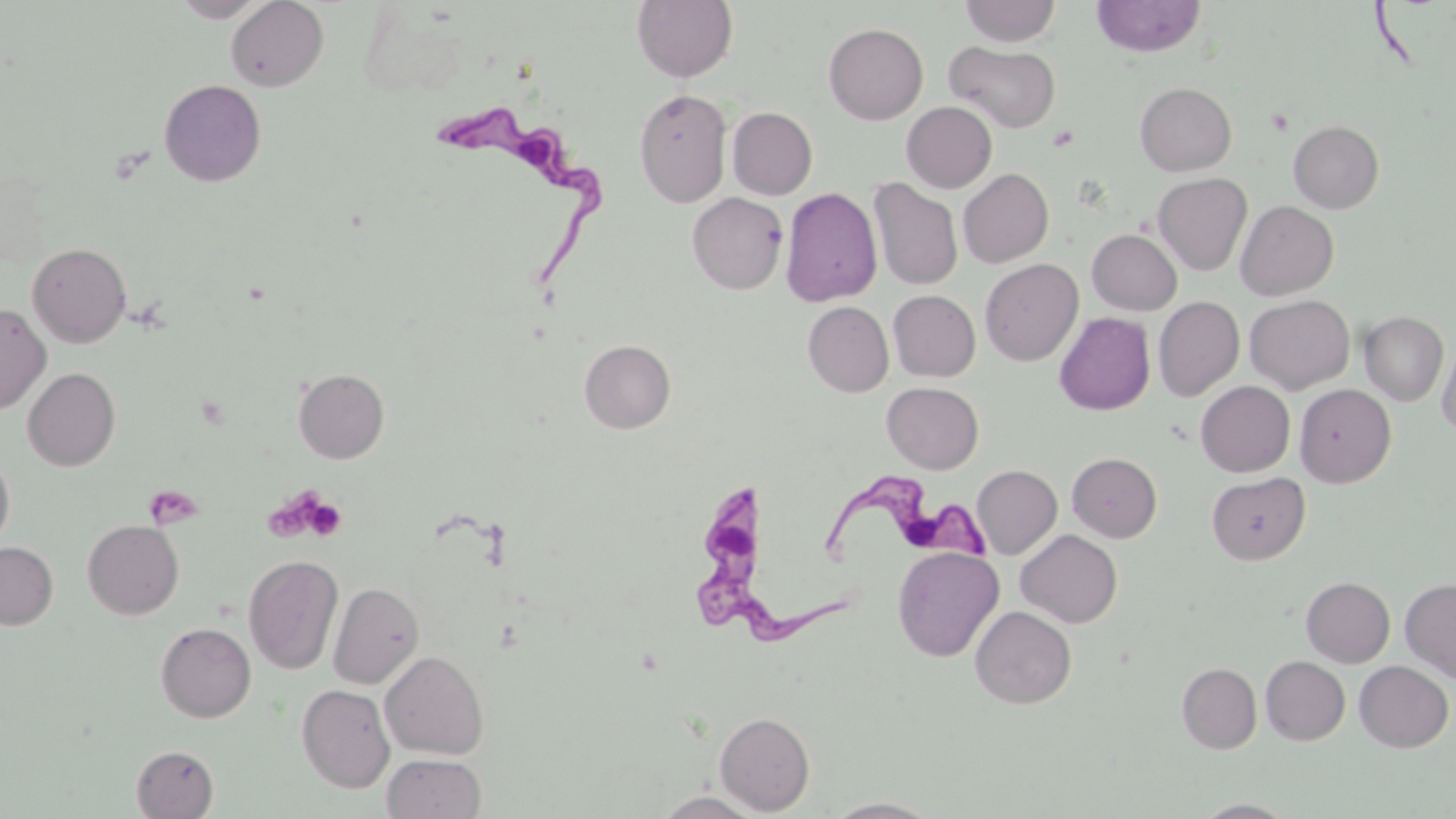
Summary:
  - Coordinate format: approximate bounding boxes as (x1, y1, x2, y2) in pixels
  - Uninfected red blood cell locations: (173, 0, 267, 22), (226, 0, 329, 91), (632, 0, 738, 83), (960, 0, 1061, 46), (1092, 0, 1206, 57), (824, 23, 928, 124), (944, 41, 1061, 133), (159, 79, 267, 187), (1135, 82, 1237, 176), (634, 88, 732, 208), (902, 101, 997, 192), (727, 107, 817, 200), (1288, 120, 1384, 213), (958, 168, 1053, 267), (1153, 173, 1252, 275), (869, 177, 963, 291), (780, 187, 882, 307), (687, 192, 788, 294), (1236, 200, 1339, 300), (1087, 229, 1182, 315), (27, 243, 131, 348), (980, 258, 1083, 366), (888, 290, 980, 381), (1244, 294, 1355, 394), (1153, 296, 1244, 401), (803, 301, 893, 397), (0, 303, 51, 414), (1054, 312, 1155, 415), (1359, 312, 1448, 406), (1437, 335, 1456, 437), (579, 339, 676, 433), (23, 367, 120, 471), (294, 368, 389, 463), (1196, 381, 1295, 477), (882, 382, 983, 473), (1294, 384, 1396, 487), (1067, 452, 1162, 542), (0, 453, 15, 551), (971, 464, 1062, 559), (1207, 472, 1310, 564), (83, 519, 183, 619), (1016, 529, 1122, 627), (0, 542, 58, 629), (892, 546, 1004, 662), (243, 554, 344, 674), (1302, 576, 1395, 667), (1400, 577, 1456, 683), (328, 581, 424, 689), (970, 605, 1076, 709), (156, 622, 256, 722), (380, 651, 489, 759), (1261, 656, 1350, 745), (1354, 661, 1453, 752), (1177, 662, 1262, 753), (297, 684, 395, 792), (715, 711, 815, 815), (131, 745, 219, 818), (382, 753, 486, 819), (652, 792, 764, 818), (824, 797, 942, 818), (1192, 799, 1299, 818)
  - Trypanosoma brucei locations: (440, 107, 606, 285), (819, 466, 988, 564), (692, 489, 845, 643)
  - Platelet locations: (1046, 125, 1079, 151), (263, 488, 336, 541), (150, 491, 212, 529), (301, 494, 346, 542)
  - Slide-level diagnosis: Trypanosoma brucei
  - Field of view: single
  - Magnification: 1000x
  - Image size: 1456×819 pixels
  - Stain: May-Grünwald-Giemsa
  - Modality: light microscopy
  - Preparation: thin blood film